Classify this cell by malaria status.
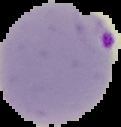

Parasitized.

image size = 121×127 pixels
image type = segmented cell region with the area outside set to black
preparation = thin blood smear